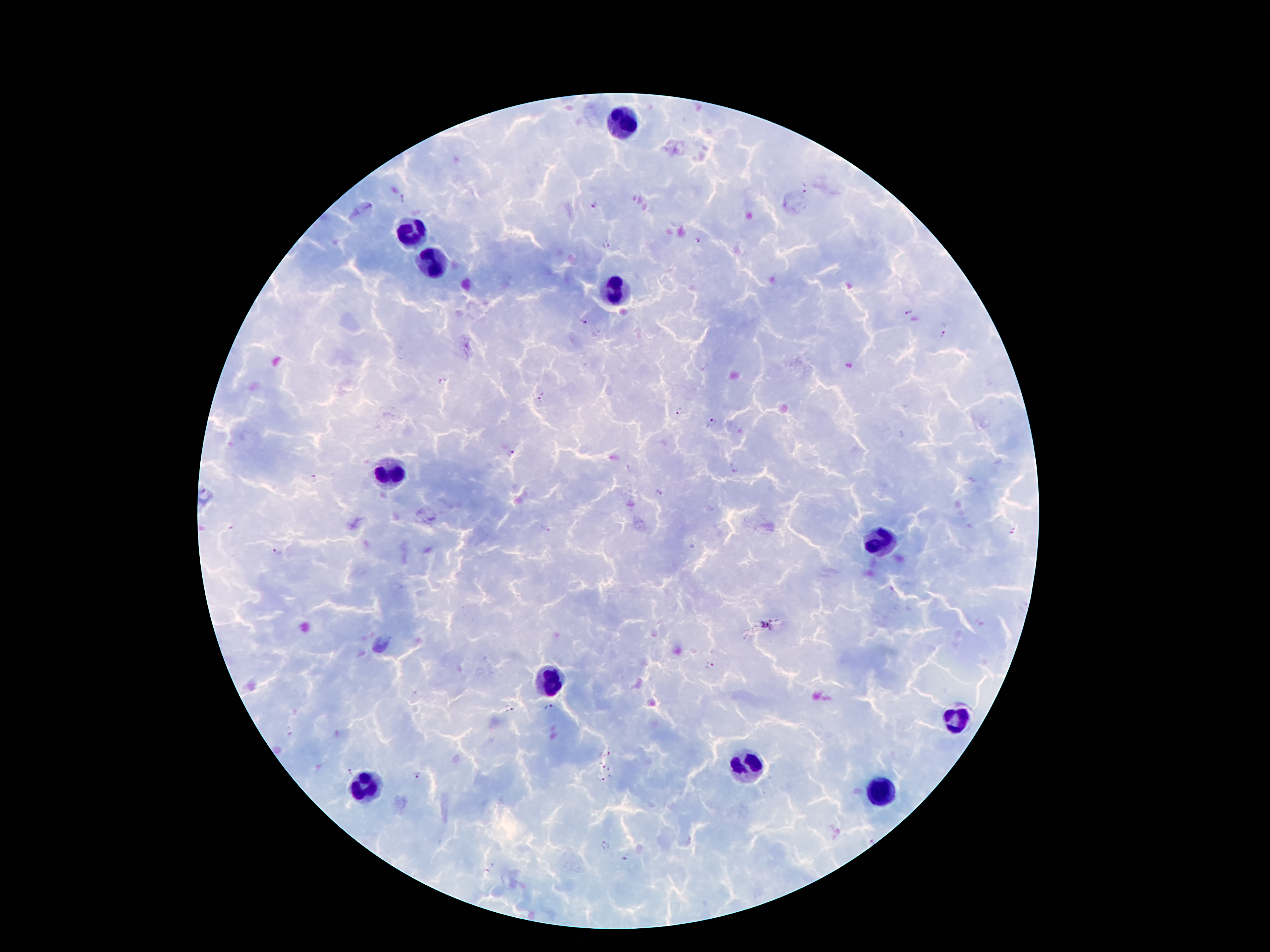
coordinate format = approximate centers as (x, y) in pixels
malaria parasite locations = (805, 186), (403, 199), (593, 204), (699, 240), (607, 243), (909, 312), (583, 322), (942, 335), (442, 381), (542, 398), (679, 413), (711, 422), (510, 454), (734, 470), (315, 478), (659, 492), (231, 525), (544, 530), (1014, 531), (277, 552), (709, 666), (549, 708), (510, 710), (606, 751), (602, 766), (610, 768), (351, 771), (417, 775), (611, 778), (600, 779), (605, 845), (626, 858)
leukocyte locations = (621, 119), (412, 235), (427, 263), (618, 294), (390, 470), (879, 541), (545, 679), (953, 720), (746, 763), (364, 787), (877, 791)
patient malaria status = infected with Plasmodium falciparum
stain = Giemsa
capture = smartphone through the microscope eyepiece
image size = 1270×952 pixels
field of view = single
preparation = thick blood film
magnification = 100x